Assess this cell for malaria.
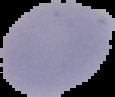

It is uninfected.

{
  "image_size": "115×97 pixels",
  "image_type": "segmented cell region with the area outside set to black",
  "preparation": "thin blood film"
}